Locate every leukocyte (white blood cell).
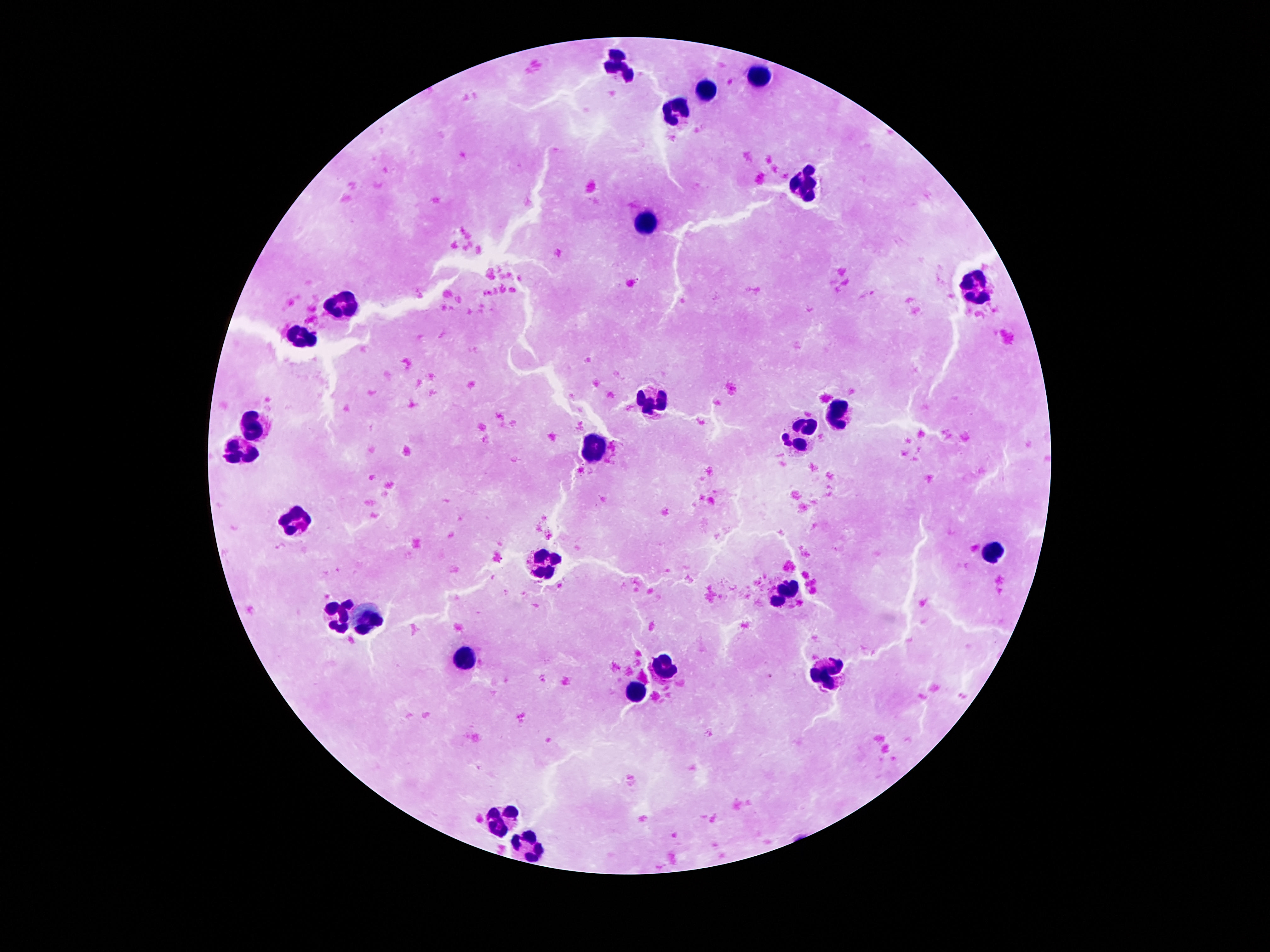
Approximate centers as [x, y] in pixels.
Leukocytes: [618, 62], [757, 73], [708, 90], [675, 112], [799, 184], [648, 223], [977, 287], [349, 300], [301, 339], [652, 400], [841, 411], [255, 421], [803, 434], [595, 449], [244, 453], [293, 523], [994, 551], [545, 557], [788, 590], [343, 614], [372, 618], [463, 660], [664, 668], [832, 672], [633, 690], [501, 813], [530, 845].

Summary:
  - Image size: 1270×952 pixels
  - Patient malaria status: uninfected
  - Field of view: single
  - Preparation: thick blood film
  - Stain: Giemsa
  - Capture: smartphone camera through the microscope eyepiece
  - Magnification: 100x